Point out each leukocyte.
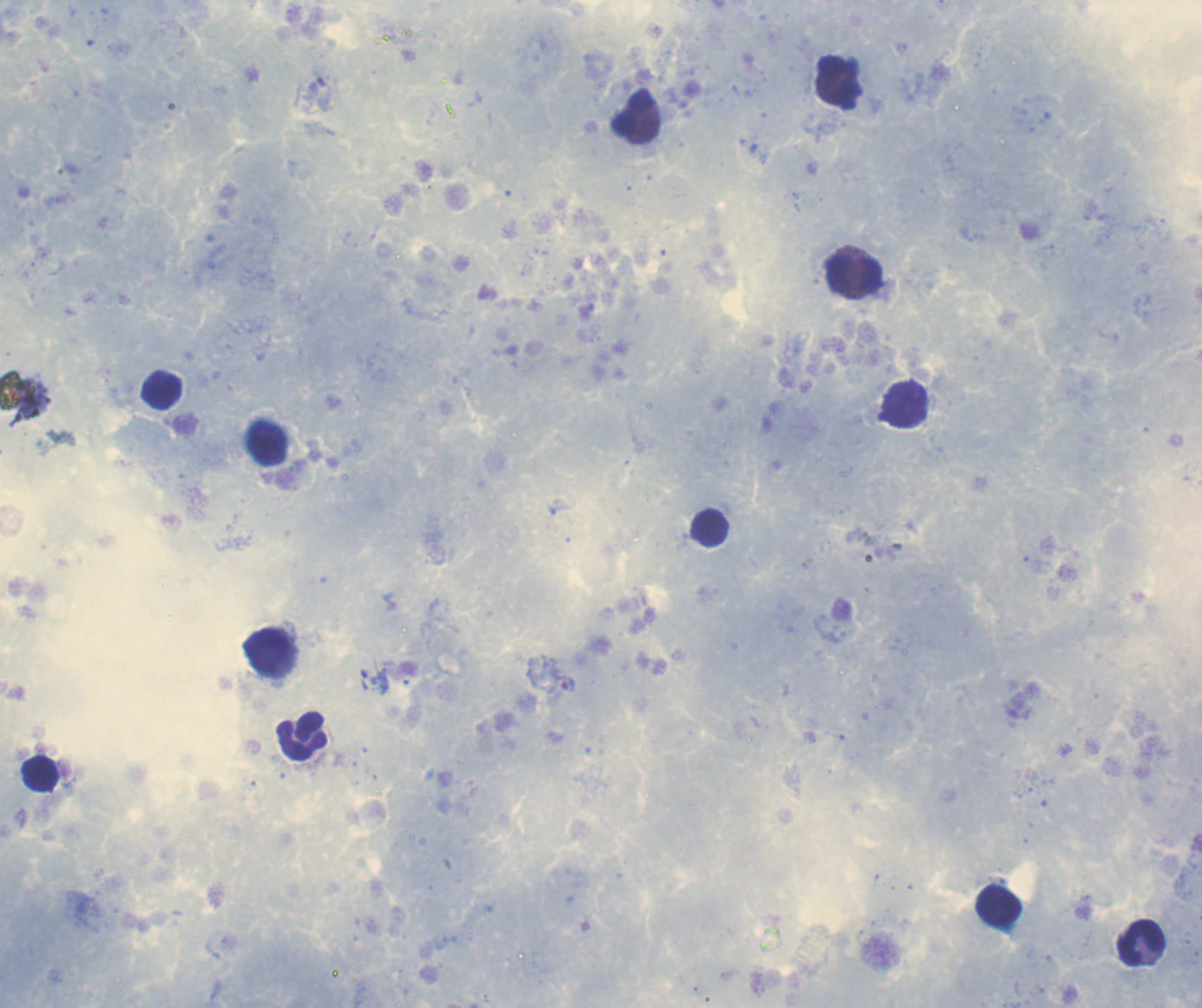

Approximate centers as {x, y} in pixels.
Leukocytes: {839, 81}, {633, 114}, {853, 275}, {161, 393}, {906, 406}, {710, 529}, {266, 653}, {303, 737}, {40, 774}, {999, 906}, {1142, 944}.

coordinate format = approximate centers as {x, y} in pixels
trophozoite locations = {374, 682}
preparation = thick blood smear
magnification = 100x
coloration quality = good
field of view = one from this slide
stain = Romanowsky
background quality = satisfactory
image size = 1202×1008 pixels
result = positive for malaria parasites
context = previously used in a real diagnosis